Locate every Plasmodium falciparum parasite and give its life-cycle stage, and locate every leukocyte and any debris.
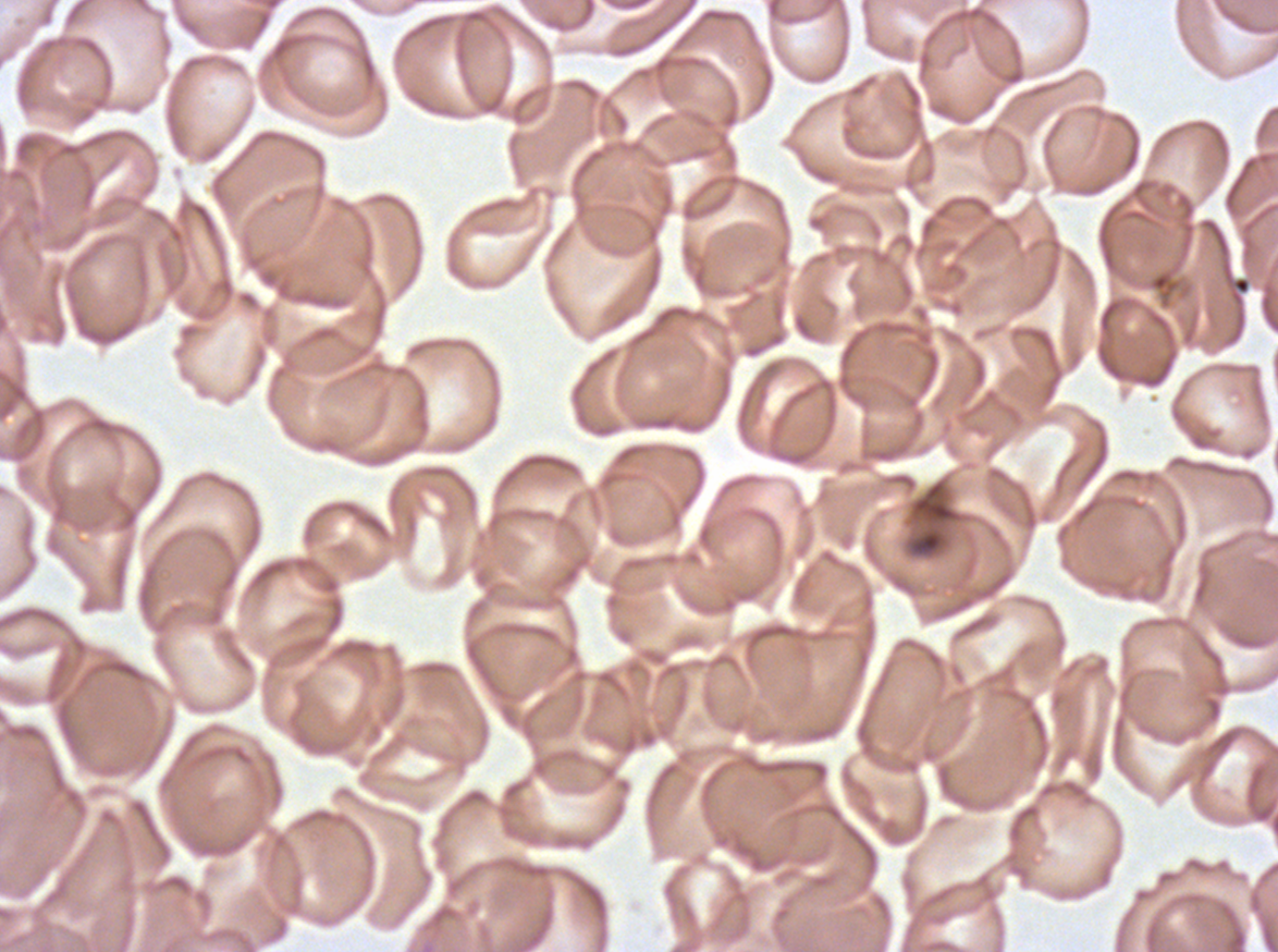
Approximate bounding boxes as [x1, y1, x2, y2] in pixels.
Debris: [919, 532, 940, 552].
No rings, late-ring/early-trophozoite forms, mid trophozoites, late trophozoites, early schizonts, late schizonts, segmenters, gametocytes, or leukocytes observed.

Thin blood smear. Giemsa-stained preparation. Plasmodium falciparum cultured ex vivo for 24 to 48 hours, from a patient in The Gambia. Image is 1278×952 pixels. A sub-image separated from a larger composite.